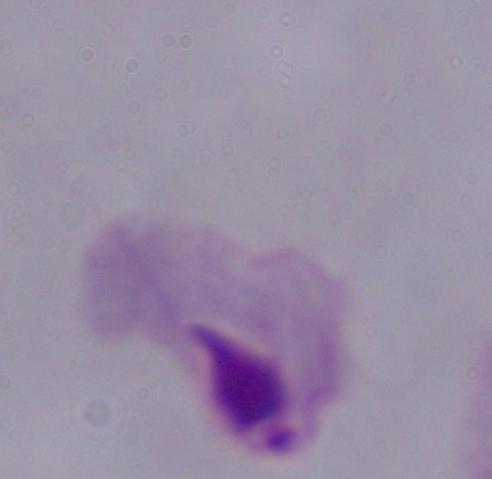

1000x magnification. A trichomonad is seen. Photomicrograph.